Classify this cell by malaria status.
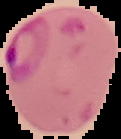

Parasitized.

Summary:
  - Image size: 121×139 pixels
  - Image type: segmented cell region with the area outside set to black
  - Preparation: thin blood smear